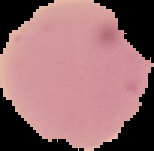
image_type: cell region segmented out of the field of view; surrounding area masked to black
malaria_status: uninfected
image_size: 154×151 pixels
preparation: thin blood film